Report the malaria status of this cell.
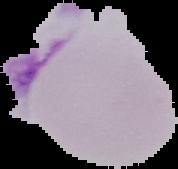
Uninfected.

Summary:
  - Image size: 178×169 pixels
  - Image type: cell region segmented out of the field of view; surrounding area masked to black
  - Preparation: thin blood film